Give the extent of all Plasmodium ovale-infected red blood cells.
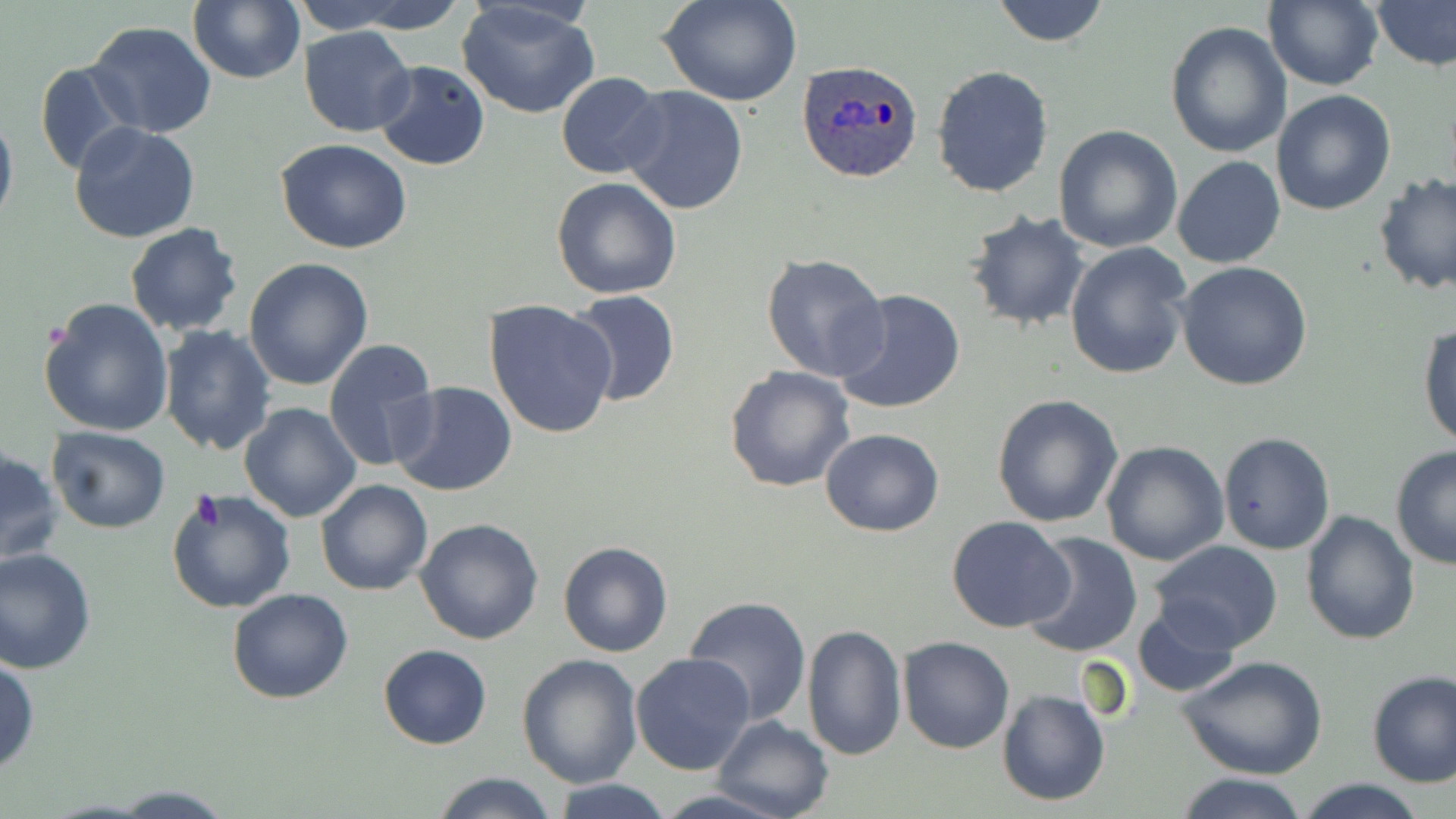
Approximate bounding boxes as [x1, y1, x2, y2] in pixels.
Plasmodium ovale-infected red blood cells: [797, 59, 926, 183].

slide_level_diagnosis: Plasmodium ovale
preparation: thin blood smear
magnification: 1000x
uninfected_red_blood_cell_locations: 'approximate bounding boxes as [x1, y1, x2, y2] in pixels: [188, 0, 306, 84], [289, 0, 420, 34], [340, 0, 470, 35], [656, 0, 805, 108], [988, 0, 1112, 47], [1263, 1, 1384, 89], [456, 2, 602, 120], [1372, 2, 1456, 73], [85, 19, 217, 139], [1165, 22, 1293, 159], [298, 26, 416, 137], [35, 59, 142, 175], [372, 60, 489, 169], [931, 66, 1055, 197], [555, 71, 668, 179], [618, 84, 748, 214], [1271, 89, 1397, 215], [0, 105, 18, 238], [68, 121, 201, 243], [1053, 124, 1183, 254], [277, 139, 413, 254], [1172, 156, 1287, 270], [1373, 174, 1455, 297], [550, 177, 682, 300], [965, 210, 1092, 332], [124, 222, 244, 338], [1064, 240, 1192, 380], [761, 253, 890, 384], [244, 257, 375, 393], [1176, 262, 1314, 390], [834, 288, 967, 414], [566, 290, 681, 409], [37, 296, 176, 436], [483, 298, 619, 439], [1418, 321, 1456, 449], [158, 326, 276, 456], [323, 339, 440, 473], [723, 365, 856, 494], [390, 382, 518, 497], [991, 392, 1123, 528], [239, 402, 362, 521], [45, 426, 171, 532], [820, 428, 945, 536], [1218, 431, 1335, 555], [1101, 440, 1229, 566], [1, 445, 64, 568], [1390, 445, 1456, 570], [315, 480, 432, 596], [165, 488, 296, 613], [1299, 510, 1420, 647], [946, 517, 1075, 634], [415, 519, 545, 645], [1022, 532, 1143, 660], [557, 540, 674, 658], [1153, 542, 1284, 653], [0, 546, 98, 672], [226, 587, 354, 705], [682, 596, 812, 725], [1132, 601, 1242, 698], [802, 624, 907, 761], [898, 635, 1013, 753], [377, 644, 491, 749], [1178, 653, 1328, 779], [516, 654, 643, 789], [630, 654, 757, 776], [0, 656, 39, 775], [1366, 669, 1456, 786], [996, 689, 1110, 807], [711, 715, 834, 819], [430, 772, 561, 818], [1178, 773, 1310, 819], [548, 778, 675, 819], [1293, 779, 1431, 818], [655, 784, 793, 819], [107, 786, 237, 817]'
modality: light microscopy
field_of_view: one of a larger specimen
image_size: 1456×819 pixels
stain: May-Grünwald-Giemsa